Give the extent of all uninfected red blood cells.
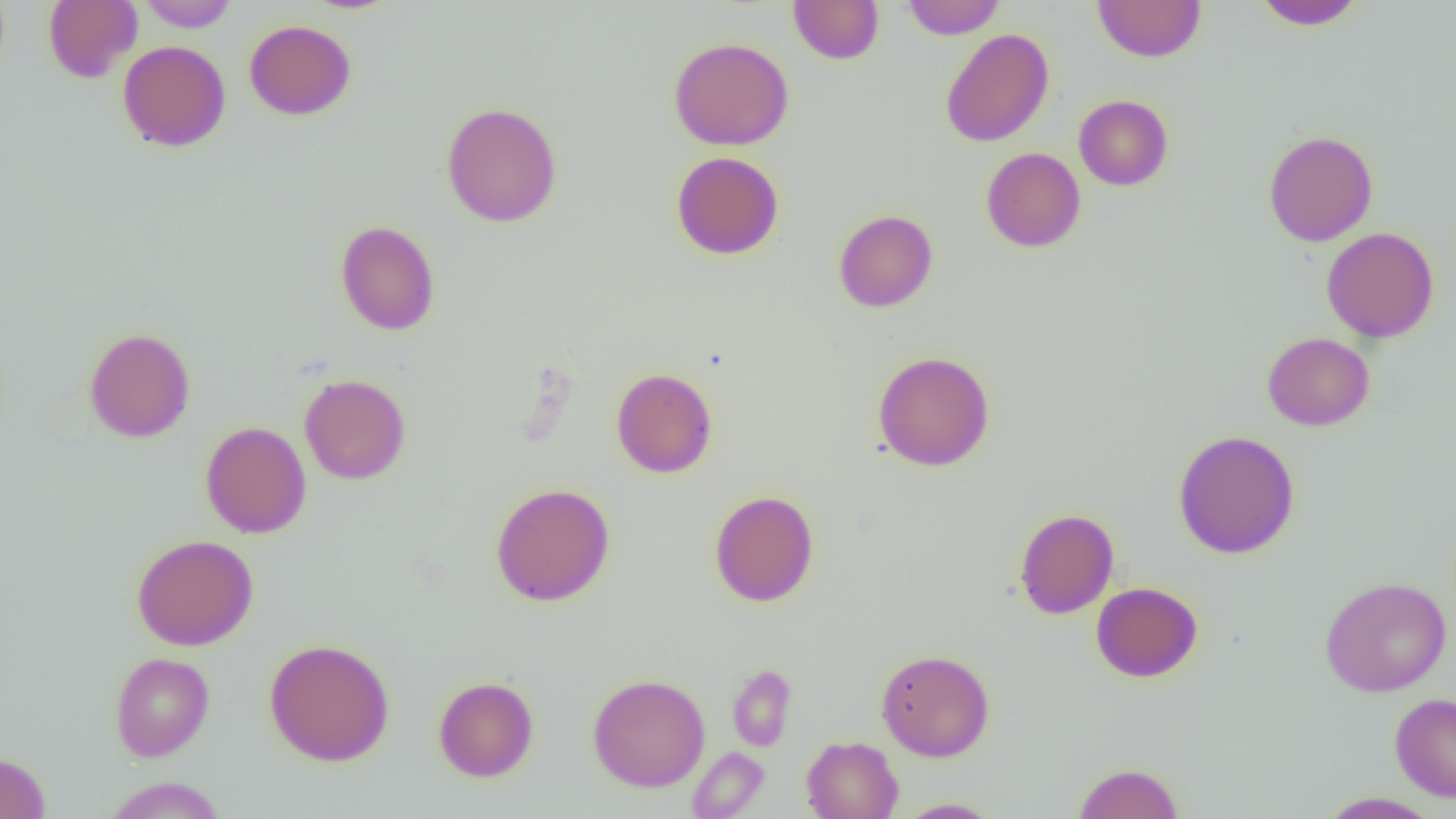
Approximate bounding boxes as [x1, y1, x2, y2] in pixels.
Uninfected red blood cells: [43, 0, 142, 83], [137, 0, 239, 32], [787, 0, 884, 65], [902, 0, 1005, 39], [1093, 1, 1206, 63], [1253, 1, 1365, 29], [244, 19, 356, 120], [940, 29, 1054, 147], [668, 36, 794, 151], [117, 40, 231, 152], [1074, 95, 1173, 190], [441, 101, 562, 228], [1263, 130, 1378, 246], [981, 147, 1086, 252], [671, 151, 784, 260], [833, 209, 938, 312], [334, 219, 440, 336], [1321, 227, 1439, 342], [84, 327, 195, 443], [1262, 332, 1375, 431], [872, 351, 995, 471], [611, 367, 718, 478], [299, 374, 411, 484], [200, 421, 311, 538], [1173, 430, 1300, 559], [490, 482, 615, 606], [709, 490, 819, 607], [1013, 508, 1119, 619], [131, 534, 259, 650], [1320, 576, 1451, 697], [1091, 581, 1203, 682], [264, 638, 395, 766], [876, 648, 995, 761], [110, 652, 215, 761], [728, 665, 797, 751], [588, 673, 710, 792], [433, 676, 539, 782], [1390, 692, 1456, 802], [801, 736, 903, 819], [687, 747, 769, 818], [0, 752, 50, 819], [1072, 762, 1184, 819], [104, 777, 227, 818], [1318, 792, 1442, 818], [893, 798, 1004, 818].

Slide-level diagnosis: no evidence of blood parasites. Image is 1456×819 pixels. 1000x magnification. Thin blood film. One field of a larger specimen. Optical microscopy.